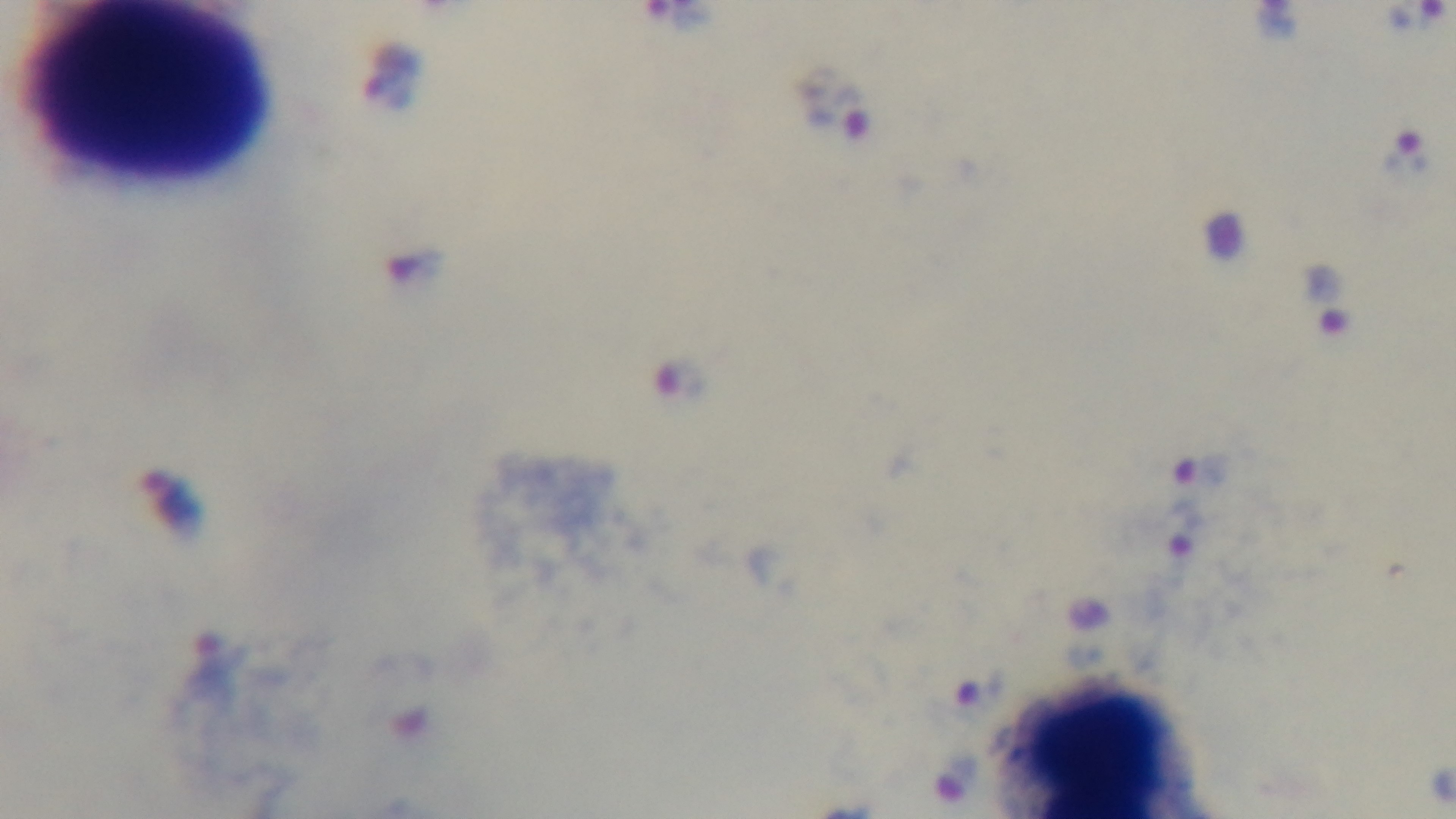

capture = mounted 4K digital camera
modality = light microscopy
objective = 100x oil immersion
stain = Giemsa
malaria status = infected
preparation = thick smear
field of view = single